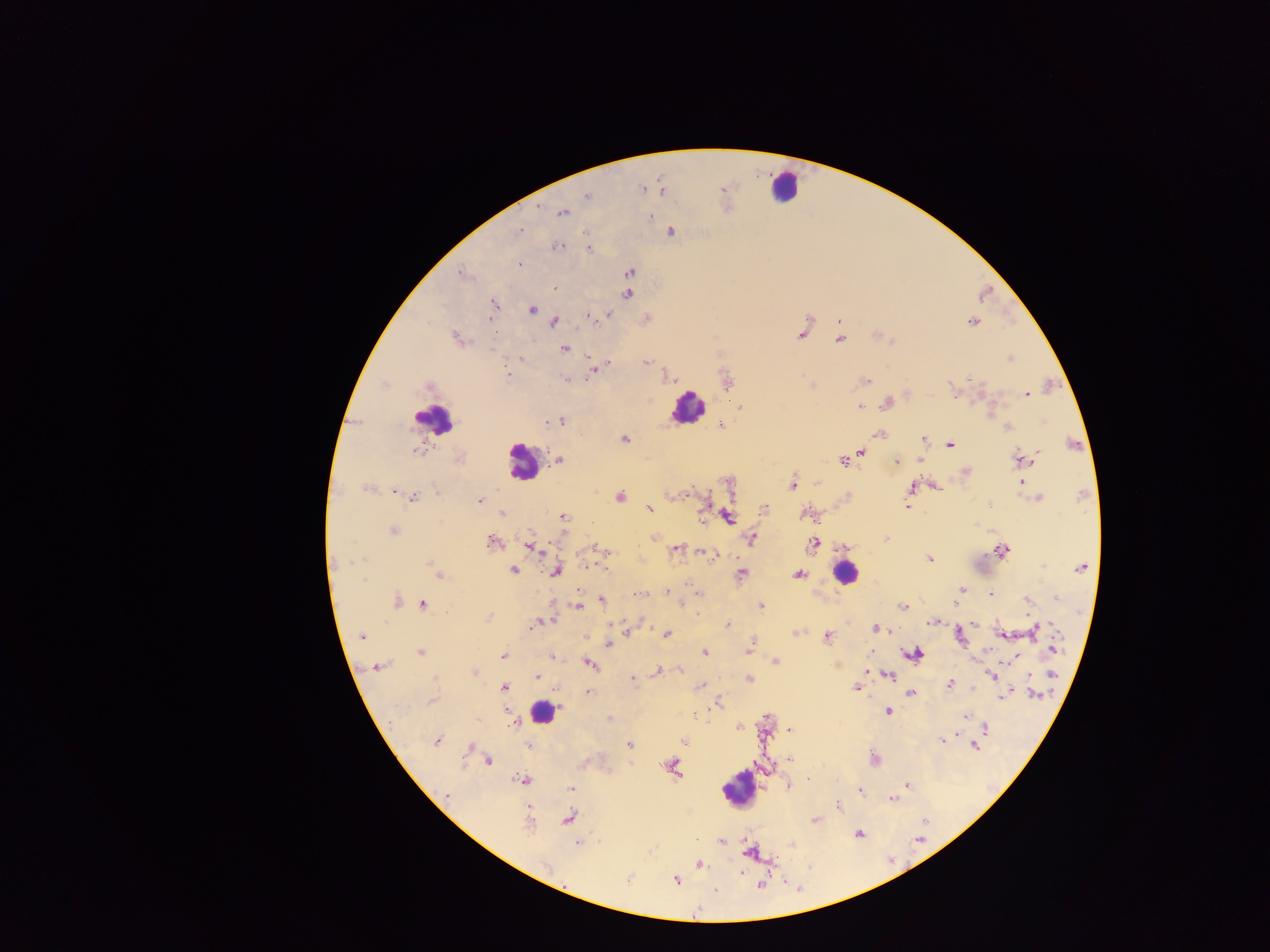
Approximate centers as [x, y] in pixels. Plasmodium parasite locations: [643, 187], [662, 189], [587, 195], [562, 212], [650, 217], [520, 231], [670, 232], [557, 246], [589, 248], [518, 264], [461, 272], [629, 272], [554, 288], [627, 293], [492, 304], [532, 309], [588, 315], [608, 315], [646, 319], [490, 320], [553, 322], [973, 322], [802, 333], [457, 339], [839, 339], [564, 348], [521, 358], [1010, 358], [646, 361], [608, 362], [592, 368], [509, 376], [666, 376], [969, 378], [566, 379], [726, 379], [865, 381], [811, 385], [954, 392], [1026, 393], [886, 402], [860, 406], [741, 407], [548, 421], [559, 421], [719, 423], [1006, 426], [881, 434], [623, 438], [923, 439], [949, 444], [417, 449], [416, 450], [861, 450], [557, 459], [920, 459], [1020, 459], [842, 461], [896, 462], [965, 473], [1022, 481], [729, 482], [818, 482], [792, 484], [934, 486], [367, 487], [910, 488], [393, 490], [413, 496], [672, 496], [620, 497], [846, 497], [1038, 498], [480, 500], [988, 504], [907, 505], [649, 509], [764, 509], [503, 514], [806, 514], [727, 517], [562, 518], [702, 518], [392, 530], [654, 537], [884, 539], [752, 540], [491, 541], [814, 542], [531, 546], [842, 547], [675, 549], [1003, 550], [701, 551], [604, 552], [929, 559], [431, 561], [1080, 567], [513, 569], [555, 571], [741, 573], [437, 574], [798, 574], [961, 589], [578, 590], [667, 591], [698, 593], [990, 593], [1055, 599], [601, 601], [1028, 601], [396, 602], [423, 604], [578, 605], [760, 606], [904, 606], [1027, 612], [488, 617], [550, 619], [935, 621], [1053, 624], [727, 625], [532, 626], [877, 629], [1033, 630], [626, 632], [796, 632], [1003, 633], [666, 634], [958, 634], [362, 636], [826, 636], [585, 637], [608, 643], [1052, 647], [749, 649], [421, 651], [703, 652], [913, 653], [503, 655], [1014, 655], [550, 657], [774, 661], [589, 664], [378, 666], [680, 669], [658, 670], [474, 672], [868, 672], [888, 675], [536, 676], [992, 676], [1028, 677], [631, 678], [748, 679], [949, 683], [700, 686], [503, 687], [856, 687], [909, 692], [588, 693], [1034, 694], [1005, 695], [432, 701], [717, 703], [505, 710], [887, 711], [964, 716], [607, 719], [513, 721], [739, 727], [985, 729], [791, 730], [437, 740], [684, 740], [940, 740], [629, 744], [974, 744], [529, 745], [471, 747], [790, 758], [874, 758], [488, 760], [671, 768], [522, 779], [806, 780], [789, 785], [907, 785], [571, 788], [859, 790], [447, 797], [891, 799], [837, 805], [527, 808], [568, 818], [814, 819], [858, 834], [720, 841], [578, 842], [790, 844], [750, 851], [698, 865], [741, 872], [628, 879], [676, 880]. Leukocyte locations: [783, 186], [688, 407], [433, 420], [521, 463], [844, 573], [542, 713], [738, 788]. Thick blood film. Image is 1270×952 pixels. Single field of view. Mobile-phone photograph taken through the microscope. Sample from Ghana.